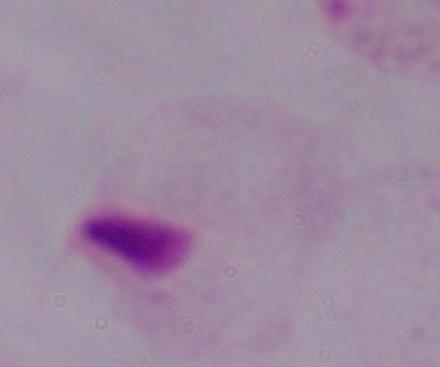
Summary:
  - Identification: trichomonad
  - Modality: photomicrograph
  - Magnification: 1000x